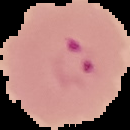
Cell region segmented out of the field of view; the surrounding area is masked to black. Malaria status: parasitized. From a thin blood film. Image is 130×130 pixels.